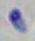

Summary:
  - Identification: Toxoplasma gondii
  - Magnification: 1000x
  - Modality: micrograph